Report the malaria status of this cell.
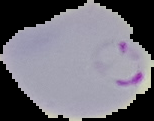
It is parasitized.

From a thin blood film. Segmented cell region on a black background. Image is 154×121 pixels.